Describe the morphology of the red blood cells.
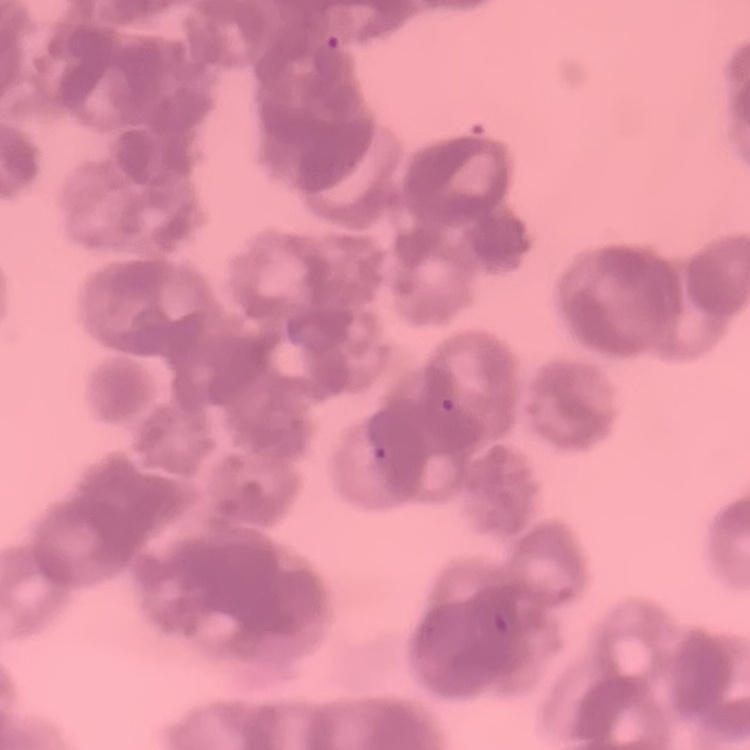

Rouleaux formation.

preparation = thin blood smear
stain = Field's or Giemsa
image type = one tile cut from a larger photomicrograph